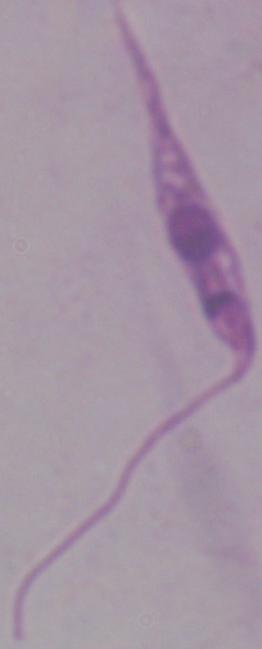

Summary:
  - Modality: photomicrograph
  - Identification: Leishmania
  - Magnification: 1000x